Name the parasite shown.
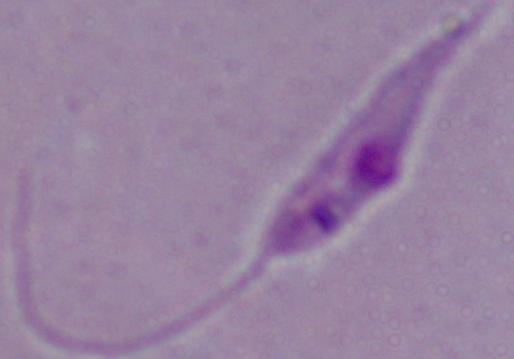
This is Leishmania.

Captured at 1000x magnification. Photomicrograph.